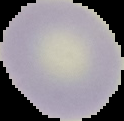 Result: no malaria parasites detected. Image is 124×121 pixels. Segmented cell region on a black background. From a thin blood film.